Identify the blood parasite species.
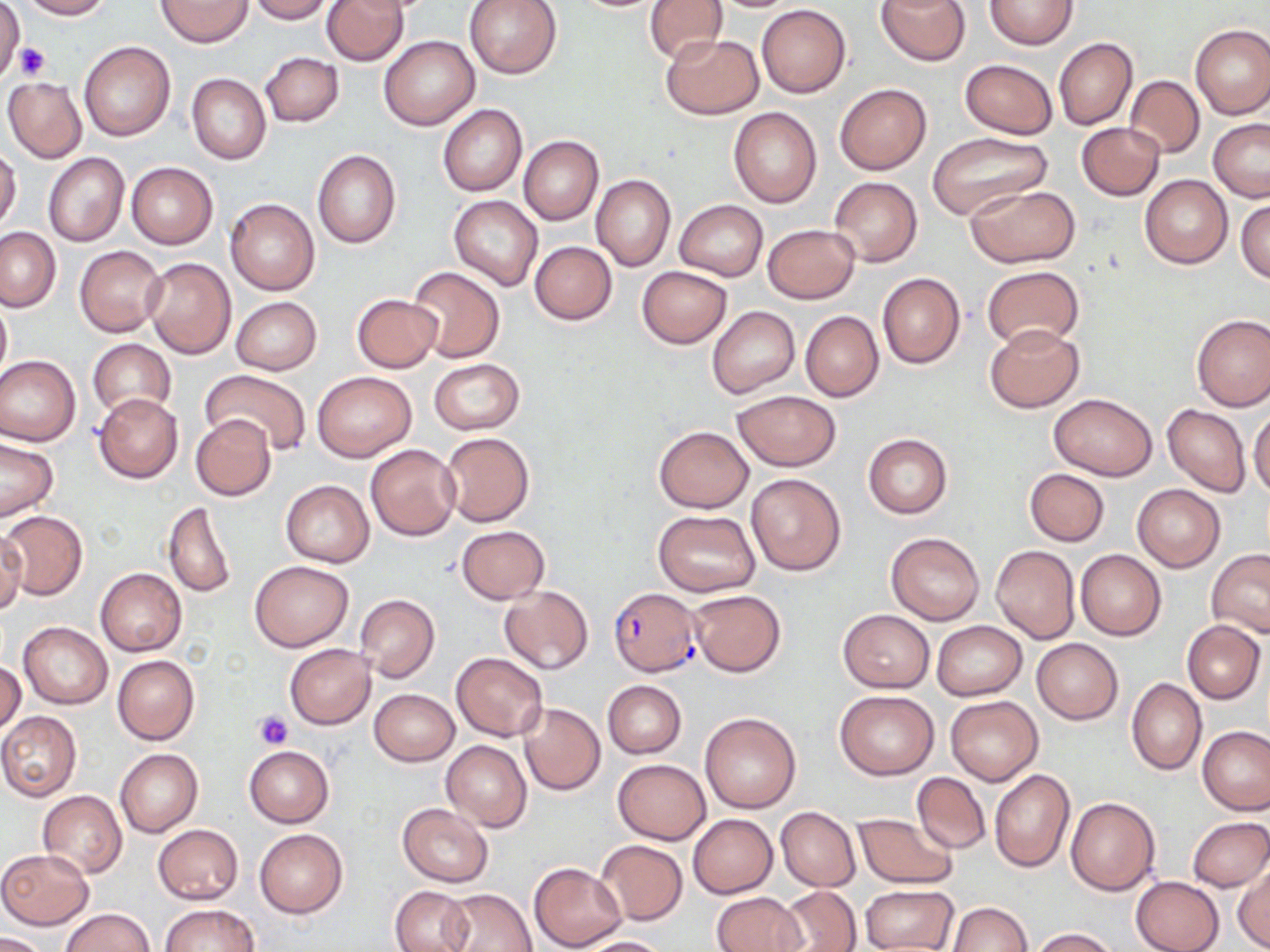
Plasmodium falciparum.

platelet locations = approximate bounding boxes as [x1, y1, x2, y2] in pixels: [16, 41, 49, 79], [255, 711, 292, 750]
stain = May-Grünwald-Giemsa
field of view = one of a larger specimen
preparation = thin blood smear
uninfected red blood cell locations = approximate bounding boxes as [x1, y1, x2, y2] in pixels: [0, 0, 24, 83], [18, 0, 112, 20], [156, 0, 253, 47], [247, 0, 333, 23], [323, 0, 408, 65], [464, 0, 563, 79], [564, 0, 672, 12], [645, 0, 729, 65], [877, 0, 969, 65], [984, 0, 1077, 50], [756, 4, 851, 97], [1190, 23, 1270, 119], [661, 33, 762, 119], [379, 35, 479, 130], [1054, 38, 1138, 129], [78, 41, 175, 141], [261, 52, 344, 126], [960, 59, 1058, 139], [186, 73, 271, 164], [1124, 75, 1204, 158], [2, 76, 86, 164], [835, 84, 932, 175], [437, 104, 527, 196], [728, 108, 822, 207], [1208, 119, 1270, 202], [1077, 122, 1164, 200], [927, 131, 1055, 224], [518, 135, 602, 225], [0, 145, 22, 232], [311, 148, 401, 249], [42, 152, 130, 247], [126, 162, 218, 249], [1139, 175, 1233, 268], [592, 176, 676, 269], [829, 177, 922, 266], [965, 184, 1080, 267], [448, 195, 543, 290], [226, 199, 319, 295], [1236, 199, 1270, 283], [674, 201, 767, 281], [763, 224, 859, 303], [0, 227, 61, 312], [530, 241, 616, 325], [74, 244, 168, 337], [143, 257, 236, 359], [982, 265, 1084, 353], [407, 266, 504, 362], [637, 266, 732, 348], [877, 272, 964, 369], [352, 294, 443, 373], [0, 296, 11, 382], [230, 297, 321, 375], [707, 306, 798, 398], [800, 310, 884, 402], [1192, 313, 1270, 412], [984, 323, 1085, 413], [88, 339, 175, 420], [0, 355, 81, 446], [429, 358, 523, 434], [313, 370, 416, 462], [201, 371, 312, 455], [731, 391, 841, 471], [93, 393, 183, 483], [1047, 393, 1158, 480], [1163, 404, 1251, 495], [1249, 407, 1270, 498], [191, 415, 276, 501], [653, 425, 754, 513], [440, 432, 534, 526], [863, 433, 953, 518], [0, 439, 59, 520], [365, 444, 460, 540], [1025, 468, 1110, 545], [746, 474, 846, 575], [281, 480, 374, 567], [1132, 484, 1225, 572], [161, 500, 237, 599], [1, 510, 88, 601], [653, 510, 761, 595], [456, 525, 550, 604], [0, 527, 26, 617], [885, 531, 984, 625], [991, 545, 1081, 643], [1075, 549, 1166, 640], [1206, 549, 1270, 638], [250, 560, 353, 651], [96, 568, 186, 656], [499, 586, 593, 674], [688, 590, 785, 676], [355, 593, 440, 682], [839, 609, 933, 692], [1182, 620, 1265, 703], [931, 621, 1027, 700], [19, 622, 112, 708], [1032, 639, 1123, 723], [285, 645, 375, 728], [452, 652, 548, 741], [112, 655, 199, 746], [0, 661, 26, 735], [1127, 678, 1206, 775], [602, 680, 686, 758], [835, 688, 939, 779], [370, 689, 459, 766], [945, 694, 1043, 785], [518, 703, 605, 796], [0, 711, 81, 801], [700, 712, 801, 812], [1197, 725, 1270, 815], [440, 740, 531, 831], [244, 746, 334, 827], [115, 749, 203, 836], [613, 759, 711, 844], [989, 769, 1074, 873], [912, 771, 990, 853], [38, 790, 127, 878], [1066, 797, 1160, 895], [398, 804, 493, 886], [775, 807, 861, 891], [852, 812, 958, 889], [689, 814, 777, 898], [1186, 816, 1270, 892], [152, 823, 244, 905], [255, 828, 347, 917], [596, 840, 688, 926], [0, 849, 93, 928], [529, 862, 626, 951], [1233, 864, 1270, 951], [1131, 876, 1224, 952], [861, 884, 957, 952], [391, 885, 474, 952], [776, 886, 862, 952], [444, 887, 536, 952], [711, 892, 807, 952], [946, 902, 1033, 952], [160, 904, 258, 952], [60, 908, 153, 952], [1029, 927, 1120, 951], [0, 932, 48, 952], [576, 937, 673, 952]
modality = optical microscopy
image size = 1270×952 pixels
Plasmodium falciparum-infected red blood cell locations = approximate bounding boxes as [x1, y1, x2, y2] in pixels: [610, 588, 700, 676]
magnification = 1000x